Identify the blood parasite species.
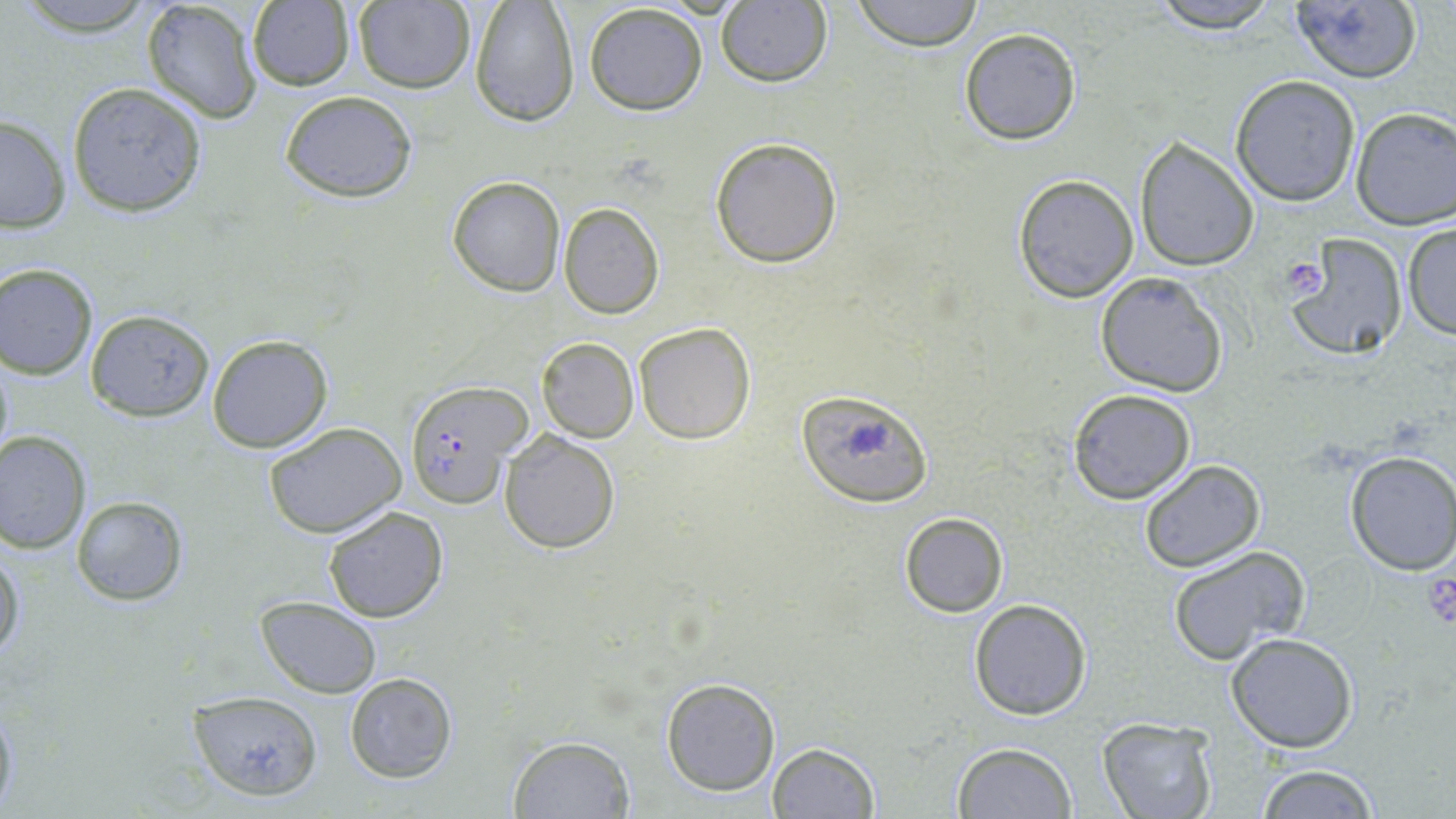
Plasmodium falciparum.

preparation = thin blood smear
field of view = single
stain = May-Grünwald-Giemsa
modality = optical microscopy
magnification = 1000x
uninfected red blood cell locations = approximate bounding boxes as (x1, y1, x2, y2) in pixels: (13, 0, 160, 37), (141, 0, 264, 124), (352, 0, 476, 94), (849, 0, 985, 50), (1145, 0, 1282, 33), (1286, 0, 1423, 84), (246, 1, 355, 92), (582, 2, 708, 116), (715, 2, 832, 87), (469, 3, 580, 127), (959, 27, 1083, 145), (1230, 75, 1362, 206), (66, 82, 208, 216), (279, 91, 418, 202), (1351, 107, 1456, 230), (0, 114, 72, 233), (709, 136, 843, 267), (1132, 136, 1259, 271), (1013, 173, 1139, 302), (446, 175, 565, 296), (558, 202, 664, 319), (1401, 222, 1456, 339), (1286, 237, 1409, 361), (1, 262, 99, 378), (1094, 271, 1229, 396), (86, 309, 215, 422), (634, 322, 756, 444), (207, 335, 334, 453), (536, 337, 638, 442), (0, 350, 14, 467), (1067, 388, 1196, 504), (798, 399, 932, 503), (262, 420, 410, 537), (0, 431, 93, 552), (499, 431, 620, 553), (1343, 451, 1456, 575), (1138, 459, 1266, 572), (71, 495, 192, 606), (322, 507, 449, 623), (898, 511, 1009, 619), (0, 541, 24, 668), (1167, 545, 1311, 664), (255, 597, 382, 698), (967, 599, 1092, 720), (1228, 634, 1359, 752), (345, 673, 458, 783), (660, 677, 781, 795), (188, 690, 322, 801), (0, 692, 18, 819), (1097, 718, 1218, 819), (507, 734, 635, 818), (951, 742, 1077, 818), (766, 743, 880, 819), (1254, 763, 1380, 819)
platelet locations = approximate bounding boxes as (x1, y1, x2, y2) in pixels: (1278, 258, 1330, 300), (1421, 560, 1456, 630)
image size = 1456×819 pixels
Plasmodium falciparum-infected red blood cell locations = approximate bounding boxes as (x1, y1, x2, y2) in pixels: (403, 381, 528, 508)